Locate every Trypanosoma brucei.
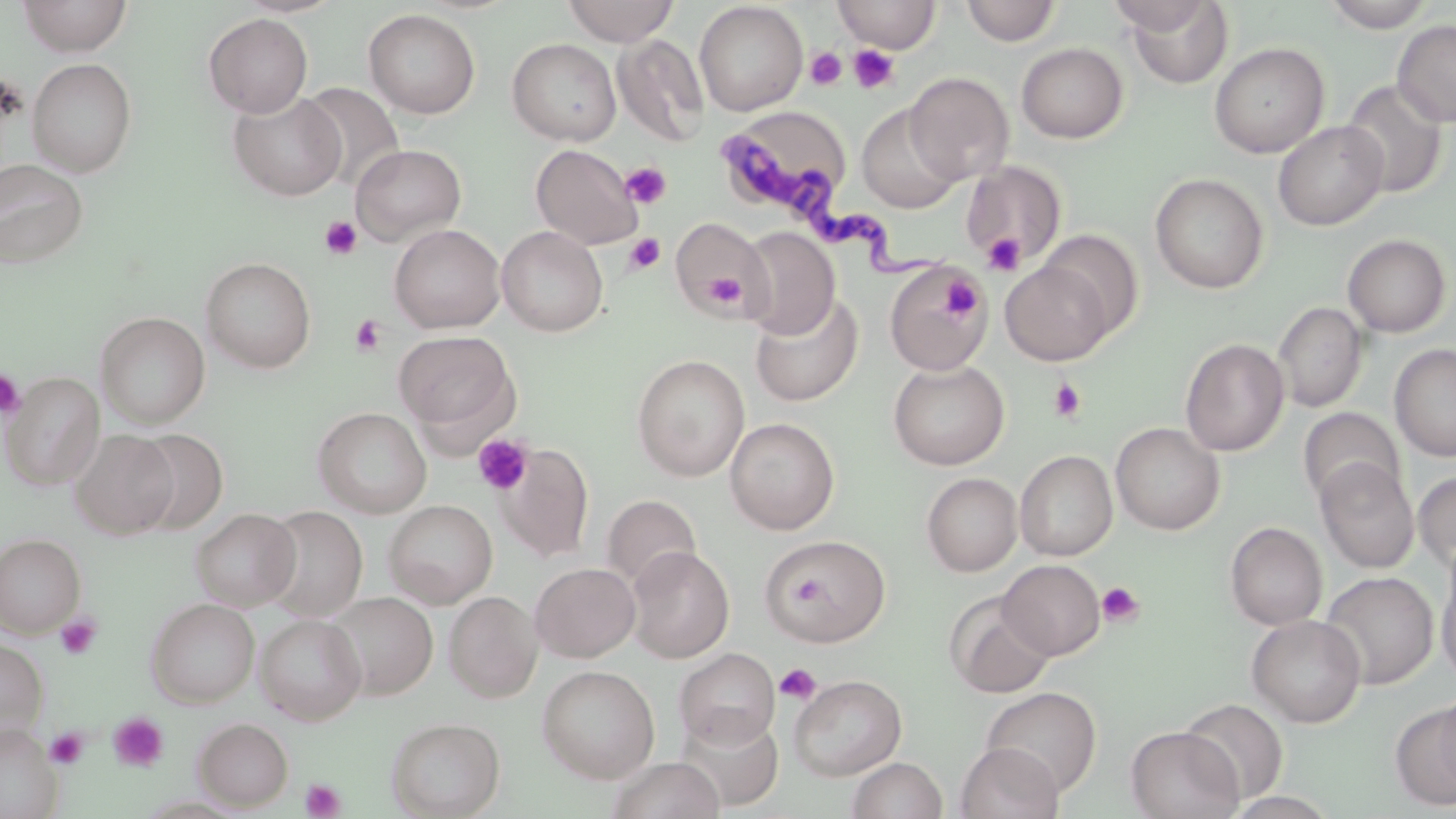

Approximate bounding boxes as [x1, y1, x2, y2] in pixels.
Trypanosoma brucei: [721, 124, 964, 286].

Platelet locations: [848, 44, 900, 94], [805, 47, 846, 91], [621, 163, 671, 208], [319, 215, 363, 259], [680, 225, 760, 316], [624, 233, 665, 274], [982, 233, 1026, 276], [704, 273, 744, 308], [940, 275, 983, 321], [350, 314, 387, 356], [0, 369, 26, 419], [1049, 378, 1087, 423], [473, 433, 534, 496], [787, 570, 827, 610], [1096, 582, 1144, 627], [55, 614, 102, 660], [775, 663, 822, 705], [109, 712, 168, 772], [46, 728, 88, 769], [300, 778, 346, 818]. Uninfected red blood cell locations: [17, 0, 133, 56], [561, 0, 681, 45], [833, 0, 941, 53], [1105, 0, 1218, 36], [694, 1, 808, 116], [962, 1, 1061, 46], [1123, 1, 1234, 88], [1322, 1, 1439, 31], [363, 9, 481, 119], [203, 13, 313, 117], [1392, 19, 1456, 127], [613, 34, 709, 147], [507, 38, 621, 145], [1209, 42, 1330, 158], [1016, 43, 1128, 143], [26, 57, 138, 177], [905, 71, 1014, 184], [1341, 79, 1447, 198], [299, 82, 405, 189], [229, 91, 346, 201], [857, 103, 965, 214], [715, 107, 851, 223], [1273, 120, 1389, 231], [351, 143, 467, 246], [530, 143, 643, 250], [0, 158, 89, 269], [961, 161, 1067, 267], [1150, 172, 1269, 293], [670, 216, 769, 317], [389, 224, 505, 333], [497, 226, 608, 336], [738, 226, 840, 339], [1037, 229, 1144, 338], [1342, 233, 1451, 338], [201, 257, 317, 373], [1000, 260, 1115, 365], [884, 262, 990, 377], [750, 294, 863, 407], [1273, 301, 1367, 413], [96, 311, 210, 429], [393, 330, 520, 442], [1180, 337, 1289, 456], [1390, 343, 1456, 463], [631, 354, 749, 481], [888, 360, 1009, 470], [2, 372, 105, 489], [312, 407, 432, 518], [1297, 407, 1404, 506], [725, 417, 840, 535], [1110, 422, 1225, 535], [129, 428, 228, 534], [70, 429, 178, 539], [495, 443, 594, 562], [1016, 449, 1117, 561], [1315, 458, 1419, 573], [1414, 470, 1456, 573], [922, 472, 1022, 576], [602, 495, 701, 592], [383, 499, 497, 608], [259, 506, 368, 621], [190, 508, 301, 611], [1225, 521, 1327, 630], [0, 534, 85, 637], [760, 536, 892, 646], [626, 546, 734, 663], [999, 559, 1105, 660], [530, 562, 640, 662], [1437, 564, 1456, 685], [1320, 571, 1439, 689], [444, 591, 542, 702], [327, 592, 438, 699], [947, 593, 1055, 699], [145, 598, 260, 707], [255, 613, 366, 725], [1247, 614, 1366, 727], [0, 641, 48, 734], [674, 648, 780, 750], [537, 665, 660, 783], [788, 673, 907, 780], [981, 686, 1102, 796], [1435, 688, 1456, 800], [1179, 698, 1290, 802], [1391, 700, 1456, 809], [674, 710, 783, 810], [386, 716, 505, 818], [193, 718, 293, 810], [0, 725, 62, 819], [1126, 726, 1243, 819], [955, 742, 1064, 819], [606, 756, 726, 819], [847, 756, 948, 819]. Slide-level diagnosis: Trypanosoma brucei. Image is 1456×819 pixels. Light microscopy. One field of a larger specimen. Thin blood film. May-Grünwald-Giemsa-stained preparation. Captured at 1000x magnification.